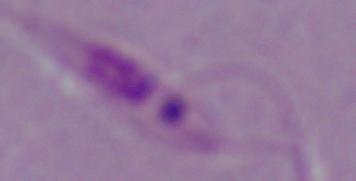

Captured at 1000x magnification. Photomicrograph. A Leishmania parasite is seen.